Comment on the morphology of the erythrocytes.
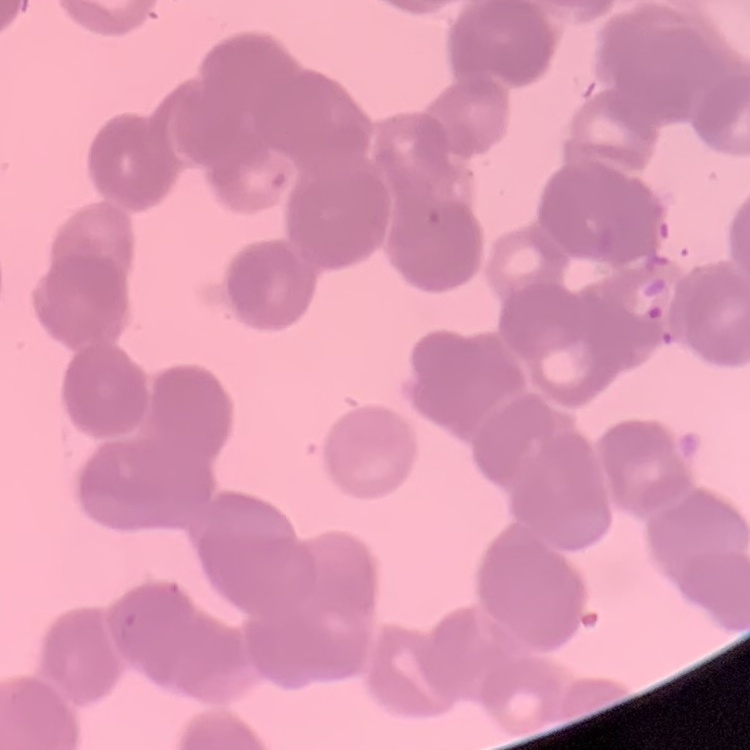

Rouleaux formation.

stain = Field's or Giemsa
preparation = thin peripheral smear
image type = one tile cut from a larger photomicrograph